Locate every blood parasite and identify its species.
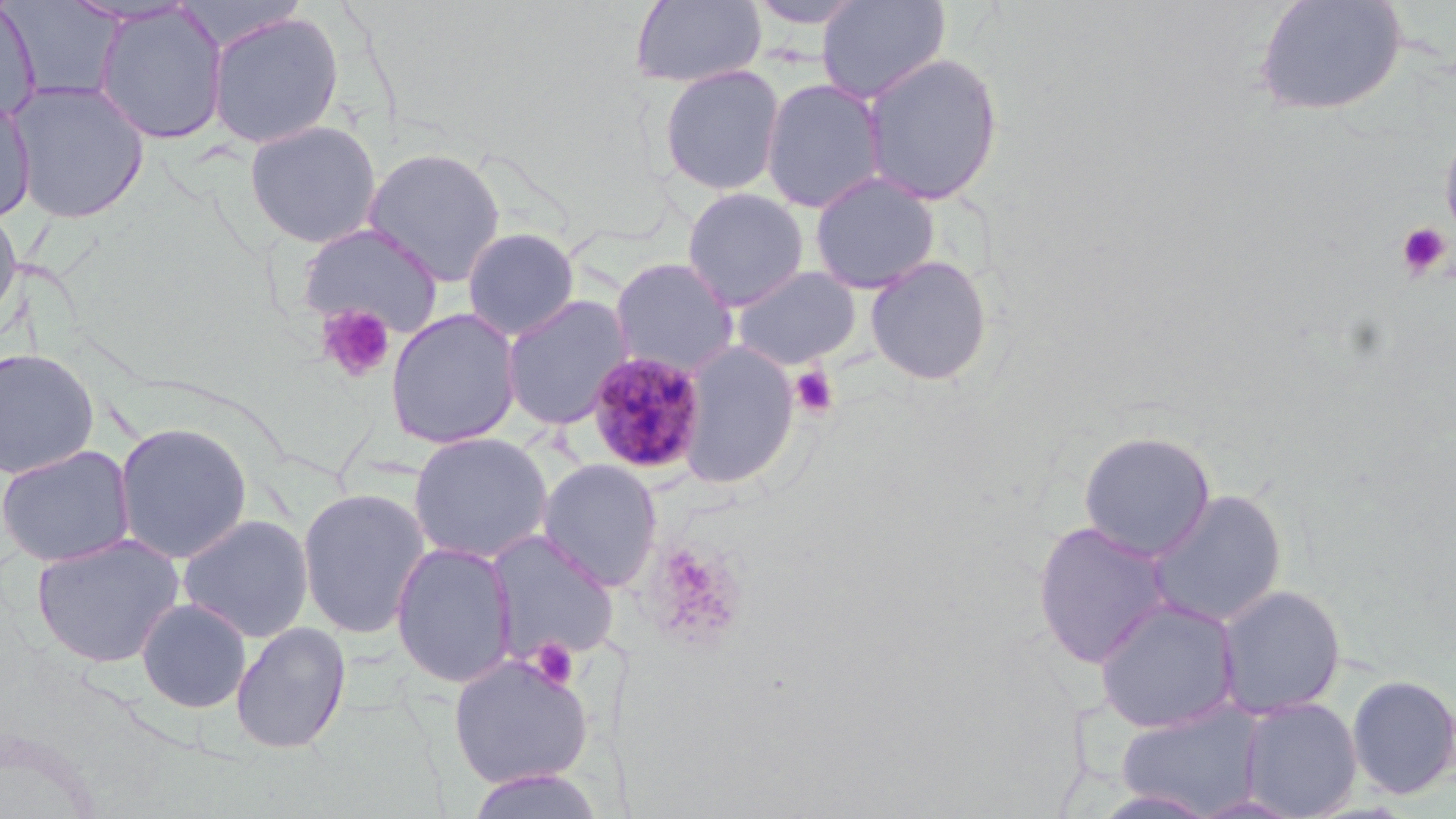

Approximate bounding boxes as (x1, y1, x2, y2) in pixels.
Plasmodium malariae-infected red blood cells: (585, 350, 710, 475).
No Plasmodium falciparum, Plasmodium ovale, Plasmodium vivax, Babesia divergens, or Trypanosoma brucei observed.

Uninfected red blood cell locations: (630, 0, 767, 89), (746, 0, 870, 29), (816, 0, 950, 104), (1252, 0, 1407, 118), (2, 1, 126, 106), (0, 4, 40, 125), (92, 5, 229, 145), (205, 9, 345, 150), (860, 51, 1004, 206), (658, 64, 786, 197), (760, 77, 886, 214), (5, 79, 151, 224), (0, 94, 36, 224), (244, 119, 382, 248), (1440, 121, 1456, 255), (363, 146, 507, 286), (808, 171, 941, 294), (681, 187, 809, 311), (0, 202, 23, 339), (296, 222, 443, 339), (461, 227, 580, 341), (864, 255, 994, 387), (610, 257, 739, 377), (730, 265, 861, 370), (500, 294, 633, 431), (384, 308, 522, 449), (679, 341, 799, 489), (0, 347, 100, 479), (113, 421, 254, 564), (1077, 430, 1216, 561), (408, 431, 553, 563), (0, 444, 136, 568), (537, 458, 663, 591), (296, 486, 432, 639), (1146, 487, 1287, 629), (177, 513, 315, 644), (1032, 519, 1173, 668), (485, 530, 620, 664), (31, 533, 185, 668), (390, 541, 517, 688), (1216, 585, 1346, 719), (1094, 596, 1241, 734), (136, 597, 252, 713), (230, 622, 351, 754), (447, 653, 594, 789), (1346, 673, 1456, 800), (1239, 697, 1362, 817), (1115, 703, 1267, 815), (463, 768, 608, 819). Platelet locations: (1396, 221, 1451, 279), (316, 304, 395, 384), (789, 365, 839, 419), (644, 543, 746, 651), (528, 638, 580, 691). Slide-level diagnosis: Plasmodium malariae. Image is 1456×819 pixels. Single field of view. Thin blood smear. 1000x magnification. May-Grünwald-Giemsa-stained preparation. Optical microscopy.